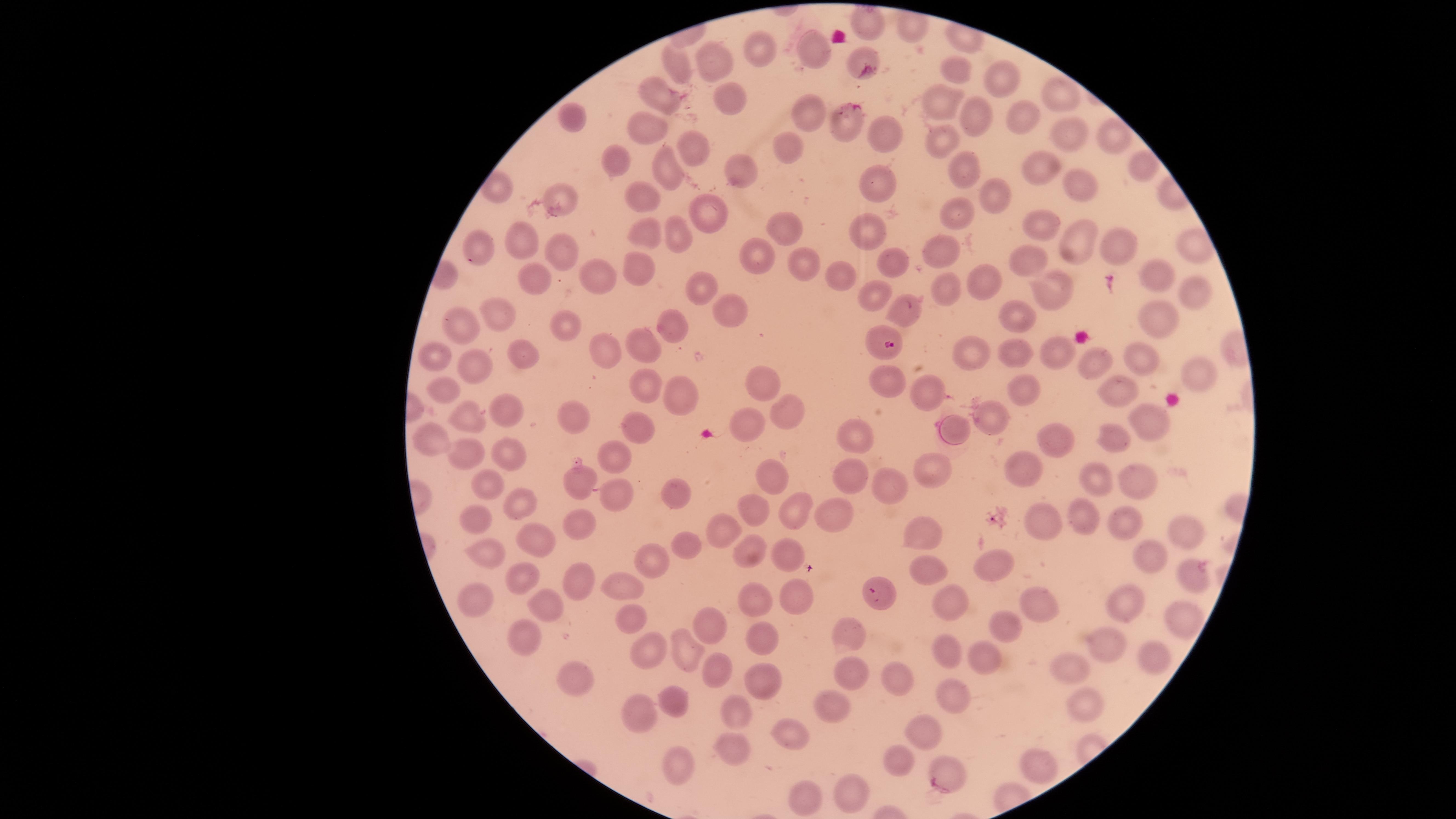

Approximate marker points, in pixels from the top-left corner. Uninfected RBCs: (x=868, y=25), (x=763, y=47), (x=811, y=48), (x=860, y=57), (x=713, y=58), (x=958, y=67), (x=673, y=69), (x=996, y=76), (x=652, y=93), (x=1057, y=95), (x=729, y=98), (x=945, y=101), (x=802, y=112), (x=978, y=113), (x=1026, y=113), (x=574, y=118), (x=842, y=127), (x=1068, y=131), (x=887, y=132), (x=649, y=133), (x=944, y=137), (x=1113, y=138), (x=690, y=145), (x=787, y=153), (x=611, y=163), (x=664, y=167), (x=960, y=170), (x=747, y=171), (x=1136, y=171), (x=1033, y=174), (x=876, y=179), (x=1090, y=187), (x=646, y=191), (x=987, y=192), (x=701, y=204), (x=561, y=207), (x=961, y=213), (x=786, y=229), (x=1040, y=229), (x=654, y=230), (x=869, y=230), (x=682, y=231), (x=1072, y=241), (x=531, y=245), (x=482, y=248), (x=1116, y=249), (x=933, y=252), (x=567, y=255), (x=754, y=256), (x=800, y=263), (x=1026, y=263), (x=892, y=270), (x=633, y=271), (x=983, y=274), (x=1151, y=274), (x=529, y=276), (x=838, y=277), (x=604, y=280), (x=948, y=287), (x=1052, y=287), (x=1187, y=289), (x=698, y=290), (x=874, y=292), (x=738, y=308), (x=904, y=309), (x=504, y=310), (x=1018, y=317), (x=463, y=323), (x=1154, y=323), (x=559, y=324), (x=665, y=324), (x=650, y=342), (x=601, y=350), (x=1012, y=352), (x=522, y=353), (x=1059, y=354), (x=1138, y=355), (x=430, y=356), (x=972, y=360), (x=1095, y=362), (x=473, y=365), (x=1188, y=369), (x=762, y=378), (x=441, y=384), (x=888, y=385), (x=641, y=389), (x=1116, y=389), (x=920, y=390), (x=1024, y=392), (x=672, y=398), (x=506, y=404), (x=779, y=410), (x=567, y=412), (x=469, y=417), (x=994, y=418), (x=634, y=422), (x=748, y=423), (x=1154, y=423), (x=853, y=434), (x=1054, y=438), (x=1114, y=444), (x=441, y=445), (x=513, y=450), (x=469, y=454), (x=613, y=458), (x=1022, y=464), (x=940, y=467), (x=851, y=473), (x=1136, y=477), (x=769, y=480), (x=574, y=482), (x=486, y=483), (x=1095, y=483), (x=895, y=486), (x=675, y=494), (x=617, y=496), (x=518, y=505), (x=749, y=508), (x=786, y=508), (x=838, y=510), (x=1082, y=520), (x=585, y=521), (x=723, y=523), (x=1123, y=524), (x=1041, y=525), (x=476, y=526), (x=1187, y=532), (x=926, y=540), (x=531, y=546), (x=691, y=548), (x=495, y=557), (x=748, y=557), (x=785, y=557), (x=645, y=560), (x=1149, y=563), (x=995, y=566), (x=1187, y=568), (x=922, y=570), (x=520, y=577), (x=623, y=582), (x=577, y=585), (x=792, y=594), (x=478, y=599), (x=945, y=599), (x=882, y=600), (x=1033, y=602), (x=1131, y=604), (x=543, y=607), (x=760, y=608), (x=1183, y=614), (x=630, y=620), (x=845, y=626), (x=704, y=627), (x=1003, y=629), (x=524, y=638), (x=762, y=644), (x=647, y=646), (x=946, y=646), (x=1106, y=647), (x=686, y=648), (x=1149, y=651), (x=978, y=666), (x=716, y=669), (x=1070, y=670), (x=856, y=677), (x=574, y=678), (x=897, y=678), (x=761, y=680), (x=951, y=698), (x=677, y=702), (x=1078, y=705), (x=829, y=706), (x=731, y=714), (x=639, y=715), (x=925, y=734), (x=792, y=737), (x=739, y=751), (x=670, y=757), (x=902, y=759), (x=1038, y=768), (x=948, y=772), (x=857, y=787), (x=808, y=802). Parasitized RBCs: (x=889, y=344). Image is 1456×819 pixels. Presence: malaria parasites detected. Circular visible region. Smartphone photograph through the microscope eyepiece. Thin smear of blood. Species: Plasmodium falciparum. Giemsa-stained preparation. Single field of view.